Assess this cell for malaria.
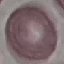
It is uninfected.

{
  "capture": "smartphone camera at the microscope eyepiece",
  "stain": "Giemsa",
  "image_type": "automatically extracted cell patch, resized to 64 × 64 pixels",
  "preparation": "thin smear"
}